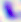
Summary:
  - Magnification: 400x
  - Modality: photomicrograph
  - Identification: Toxoplasma gondii